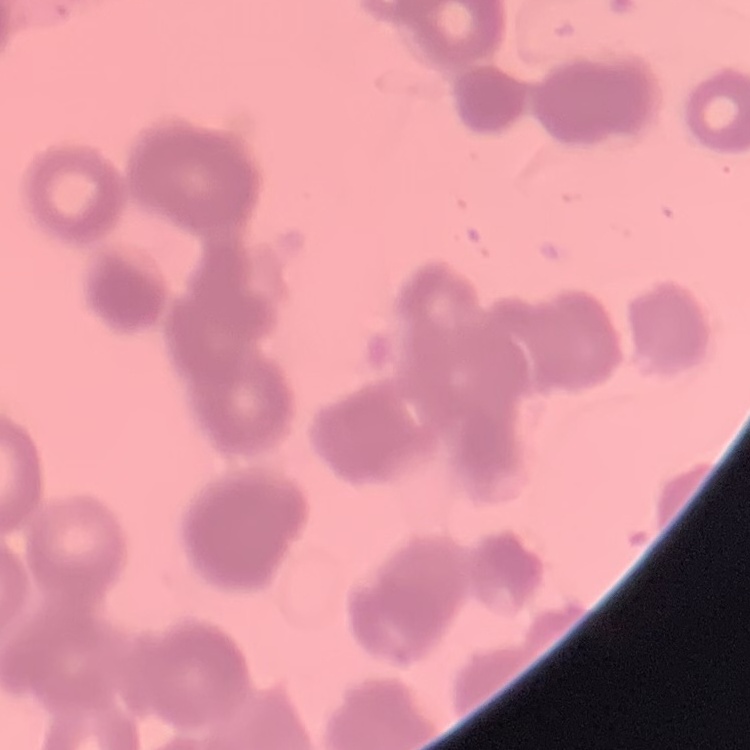
The red blood cells exhibit rouleaux formation. Stained with either Field's or Giemsa. One tile cut from a larger photomicrograph. Thin blood film.